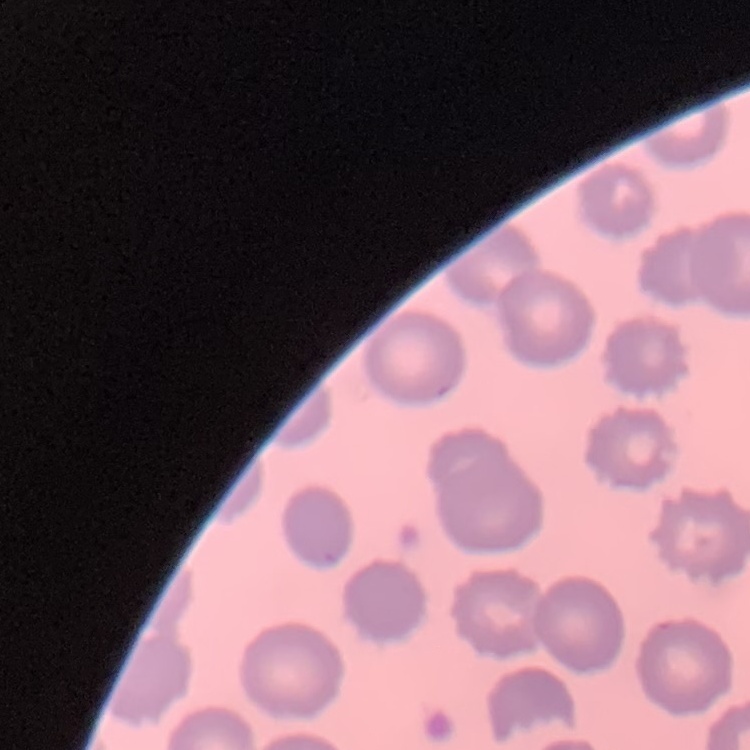

red blood cell morphology = no rouleaux formation
image type = one tile cut from a larger photomicrograph
preparation = thin blood film
stain = Field's or Giemsa